Name the parasite shown.
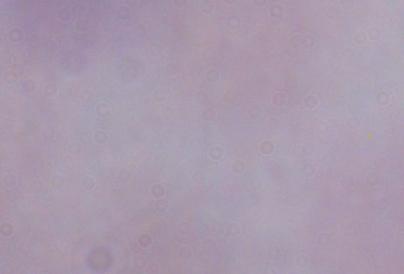

A trypanosome.

modality = micrograph
magnification = 1000x